Assess the morphology of the red blood cells.
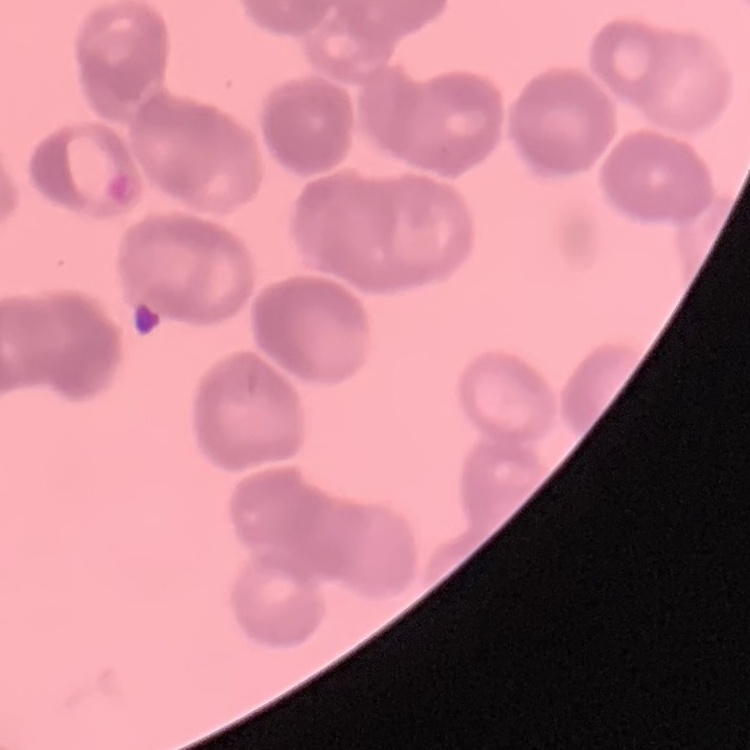
Rouleaux formation.

Summary:
  - Preparation: thin peripheral smear
  - Image type: square crop of a larger photomicrograph
  - Stain: Field's or Giemsa